Report the malaria status of this cell.
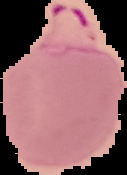

Parasitized.

The area outside the segmented cell region is set to black. Image is 127×175 pixels. From a thin blood smear.